Identify the blood parasite species.
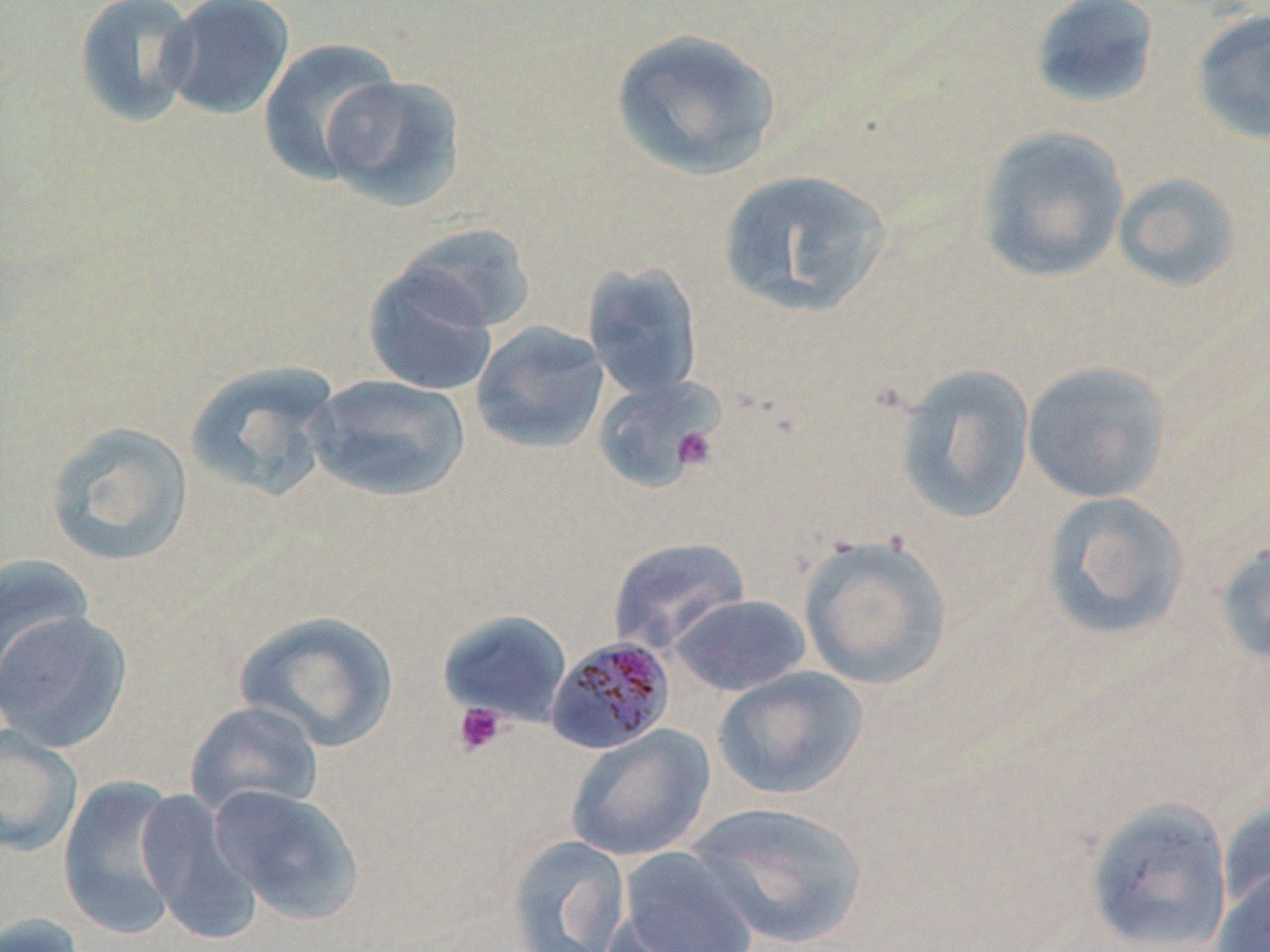

Plasmodium malariae.

Approximate bounding boxes as (x1, y1, x2, y2) in pixels. Uninfected red blood cell locations: (73, 0, 201, 127), (1028, 0, 1161, 110), (159, 1, 295, 120), (1190, 7, 1270, 147), (610, 27, 783, 181), (257, 38, 402, 185), (320, 73, 467, 212), (974, 125, 1129, 283), (717, 168, 893, 318), (1111, 171, 1242, 294), (393, 222, 537, 334), (582, 261, 703, 400), (362, 262, 499, 396), (471, 321, 609, 453), (185, 361, 342, 503), (1021, 361, 1171, 504), (893, 362, 1036, 524), (307, 374, 471, 503), (592, 375, 724, 493), (44, 421, 194, 567), (1041, 492, 1191, 641), (798, 533, 955, 691), (606, 536, 752, 655), (1213, 538, 1270, 670), (0, 554, 95, 698), (669, 594, 811, 696), (234, 609, 400, 752), (437, 609, 573, 727), (1, 610, 134, 752), (712, 667, 868, 800), (184, 701, 325, 818), (565, 723, 715, 863), (0, 724, 84, 858), (57, 775, 186, 941), (208, 784, 364, 925), (136, 788, 263, 944), (1083, 797, 1233, 952), (1218, 797, 1270, 920), (685, 801, 870, 949), (505, 835, 631, 952), (614, 846, 760, 952), (1211, 868, 1269, 952), (1, 912, 87, 952). Plasmodium malariae-infected red blood cell locations: (545, 635, 676, 754). Platelet locations: (673, 426, 718, 472), (452, 701, 507, 757). Light microscopy. May-Grünwald-Giemsa stain. 1000x magnification. Single field of view. Image is 1270×952 pixels. Thin blood film.